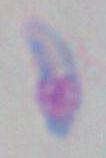
{
  "magnification": "1000x",
  "identification": "Toxoplasma gondii",
  "modality": "micrograph"
}